Point out each leukocyte.
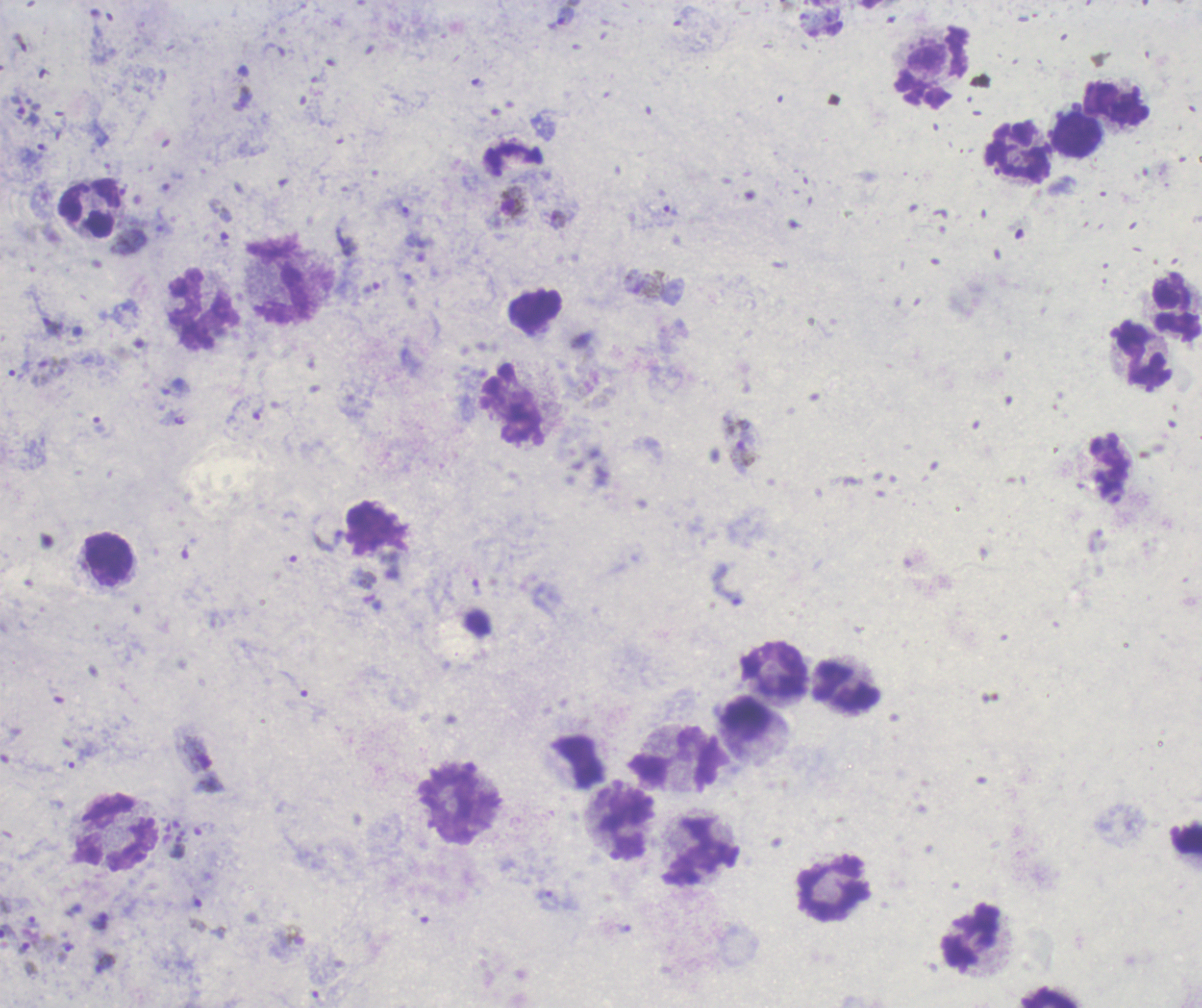
Approximate centers as {x, y} in pixels.
Leukocytes: {1116, 103}, {1075, 136}, {1020, 154}, {90, 207}, {282, 280}, {202, 309}, {1175, 309}, {1144, 355}, {514, 408}, {108, 559}, {775, 669}, {846, 686}, {675, 760}, {461, 805}, {624, 823}, {118, 834}, {1185, 836}, {701, 850}, {833, 889}, {970, 936}, {1049, 997}.

Approximate centers as {x, y} in pixels. Trophozoite locations: {565, 16}, {403, 210}, {672, 211}, {558, 219}, {53, 327}, {52, 366}, {19, 371}, {99, 425}, {327, 540}, {476, 588}, {177, 847}, {556, 901}, {32, 922}, {67, 946}, {23, 948}, {105, 962}. Gametocyte locations: {514, 202}, {649, 285}, {742, 443}, {198, 753}, {294, 935}. Life-cycle stages observed: trophozoite, gametocyte. Result: positive for Plasmodium parasites. Romanowsky stain. Thick smear of blood. Captured at 100x magnification. Image is 1202×1008 pixels. Single field of view. Background quality: unsatisfactory. Previously used in a real diagnosis.